Assess this cell for malaria.
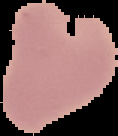

It is uninfected.

Image is 118×136 pixels. The area outside the segmented cell region is set to black. From a thin blood smear.